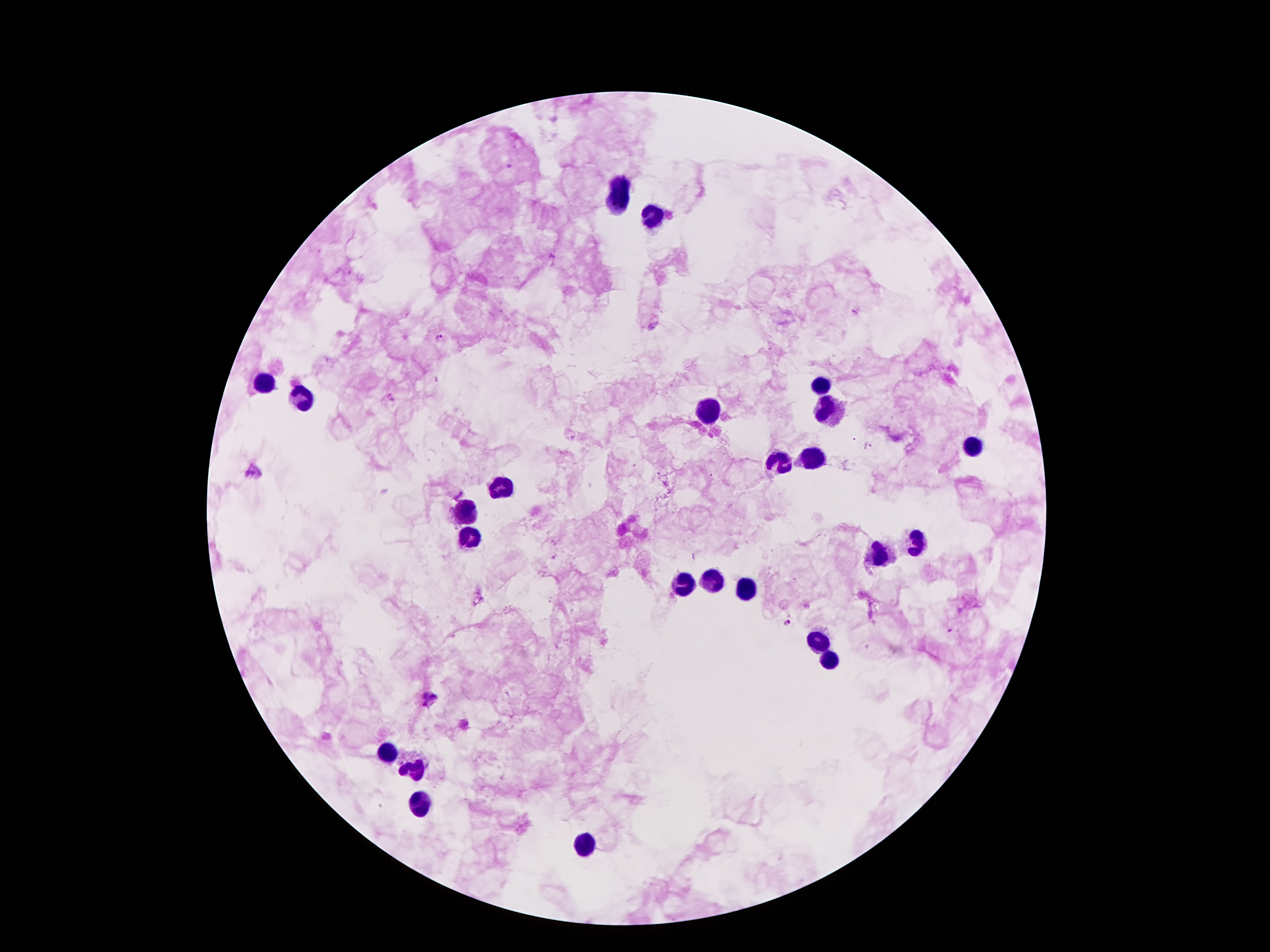

Approximate centers as {x, y} in pixels.
Summary:
  - Leukocyte locations: {624, 180}, {615, 201}, {653, 218}, {262, 382}, {817, 388}, {302, 400}, {825, 402}, {712, 409}, {970, 447}, {813, 461}, {779, 462}, {500, 484}, {466, 514}, {468, 537}, {916, 541}, {878, 553}, {712, 581}, {682, 586}, {745, 590}, {815, 640}, {829, 659}, {388, 753}, {416, 770}, {420, 805}, {586, 844}
  - Malaria parasite locations: {856, 314}, {439, 337}, {869, 446}, {786, 622}, {429, 698}
  - Preparation: thick peripheral-blood smear
  - Field of view: one from this slide
  - Patient malaria status: positive for Plasmodium falciparum
  - Capture: smartphone through the microscope eyepiece
  - Stain: Giemsa
  - Magnification: 100x
  - Image size: 1270×952 pixels